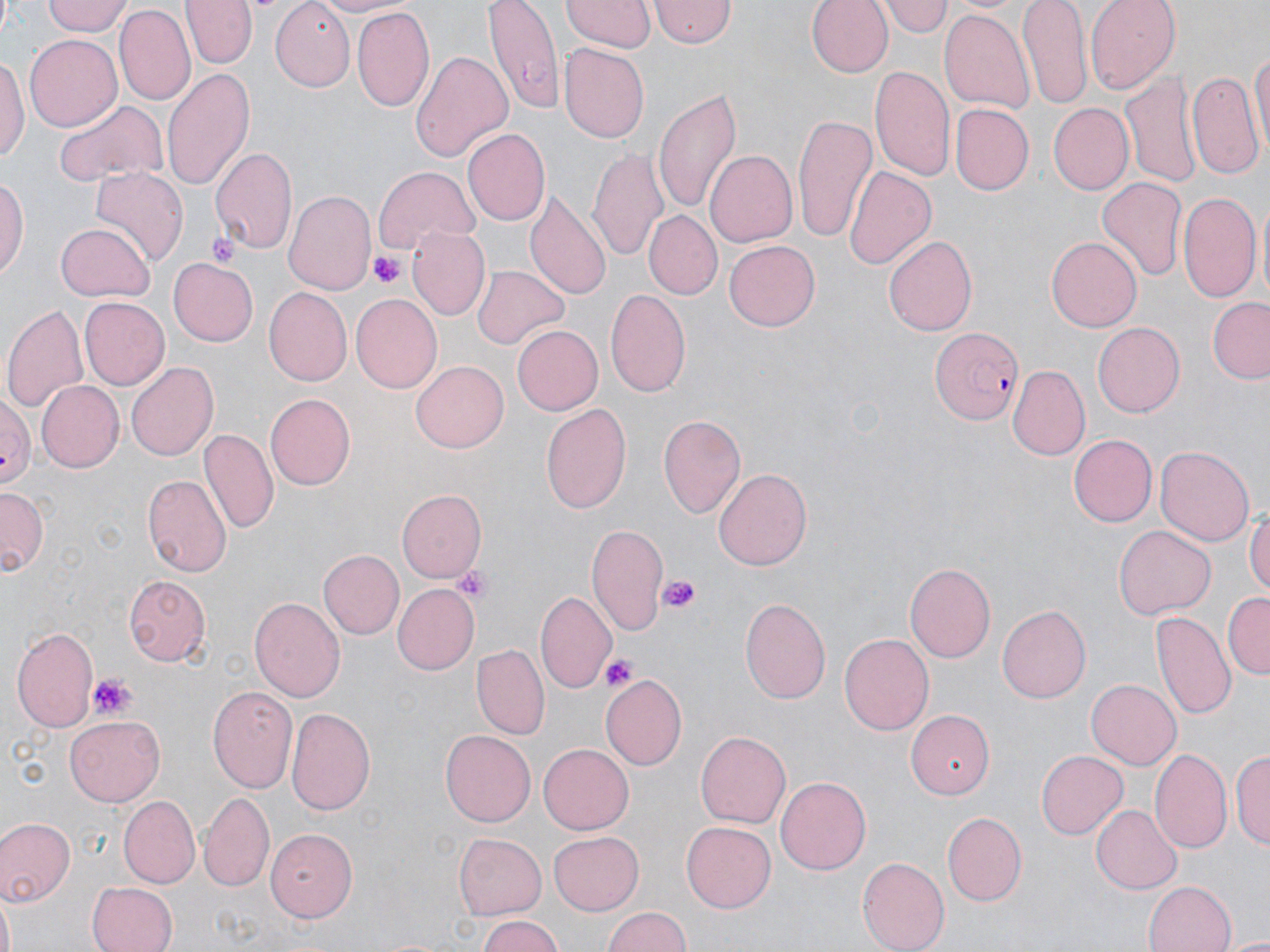 Approximate bounding boxes as (x1, y1, x2, y2) in pixels. Platelet locations: (209, 231, 240, 268), (371, 252, 404, 289), (454, 567, 492, 603), (655, 573, 703, 615), (599, 654, 637, 691), (89, 671, 136, 720). Plasmodium falciparum-infected red blood cell locations: (931, 325, 1023, 426). Uninfected red blood cell locations: (42, 0, 131, 38), (183, 0, 257, 68), (268, 0, 355, 92), (309, 0, 412, 16), (485, 0, 563, 113), (652, 0, 733, 50), (805, 0, 893, 77), (882, 0, 951, 36), (1019, 0, 1092, 111), (1086, 0, 1180, 92), (562, 1, 652, 53), (114, 7, 193, 107), (352, 7, 434, 114), (940, 8, 1036, 115), (24, 33, 122, 131), (1249, 42, 1269, 163), (557, 44, 649, 142), (410, 50, 513, 163), (0, 57, 27, 164), (161, 64, 254, 192), (870, 66, 956, 185), (1122, 69, 1203, 190), (1186, 69, 1262, 177), (654, 90, 741, 213), (53, 99, 165, 190), (1047, 104, 1132, 195), (950, 105, 1033, 196), (791, 115, 874, 240), (463, 128, 550, 227), (209, 145, 298, 253), (589, 148, 670, 262), (705, 151, 797, 247), (371, 165, 482, 259), (91, 166, 186, 261), (843, 166, 935, 271), (1, 173, 28, 284), (1096, 177, 1188, 286), (283, 188, 376, 297), (525, 191, 611, 302), (1179, 191, 1261, 305), (645, 210, 721, 297), (56, 223, 154, 301), (408, 225, 490, 322), (882, 234, 976, 337), (1046, 236, 1142, 332), (725, 240, 819, 332), (168, 255, 259, 344), (472, 265, 568, 349), (262, 289, 351, 387), (605, 290, 691, 399), (351, 294, 442, 393), (78, 296, 169, 390), (1208, 297, 1270, 384), (3, 301, 90, 418), (1092, 322, 1185, 417), (512, 324, 602, 417), (411, 360, 510, 454), (127, 361, 218, 462), (1009, 366, 1089, 458), (36, 381, 123, 471), (0, 389, 35, 496), (264, 391, 355, 487), (541, 402, 631, 513), (659, 415, 745, 520), (200, 429, 278, 536), (1069, 434, 1156, 526), (1155, 445, 1255, 546), (714, 467, 813, 569), (142, 473, 231, 577), (0, 488, 45, 575), (395, 490, 485, 584), (1246, 504, 1270, 601), (586, 523, 670, 638), (1114, 524, 1216, 619), (317, 550, 403, 639), (904, 562, 997, 663), (122, 578, 207, 666), (391, 583, 479, 675), (537, 591, 616, 691), (1224, 592, 1269, 678), (740, 595, 831, 705), (249, 596, 343, 702), (997, 605, 1090, 703), (1151, 610, 1234, 720), (11, 624, 100, 733), (838, 633, 934, 736), (474, 645, 547, 738), (600, 674, 686, 772), (1086, 679, 1181, 770), (208, 684, 299, 794), (287, 707, 376, 817), (906, 708, 993, 798), (65, 717, 167, 807), (439, 727, 533, 825), (695, 730, 790, 828), (538, 744, 635, 834), (1186, 747, 1267, 853), (1151, 748, 1231, 856), (1230, 748, 1269, 851), (1037, 752, 1127, 839), (774, 776, 870, 875), (198, 793, 274, 891), (120, 797, 199, 886), (1091, 804, 1181, 893), (943, 811, 1025, 907), (0, 817, 75, 903), (680, 821, 777, 913), (265, 828, 357, 923), (549, 828, 644, 913), (454, 833, 546, 917), (856, 856, 949, 951), (1144, 880, 1236, 952), (87, 882, 178, 952), (1, 889, 17, 952), (602, 907, 694, 952), (475, 914, 564, 952), (1225, 934, 1270, 950). Slide-level diagnosis: Plasmodium falciparum. Captured at 1000x magnification. Single field of view. Image is 1270×952 pixels. Thin blood smear. May-Grünwald-Giemsa stain. Optical microscopy.